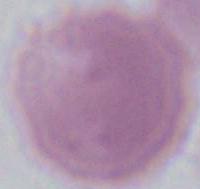

Summary:
  - Modality: photomicrograph
  - Identification: red blood cell
  - Magnification: 1000x